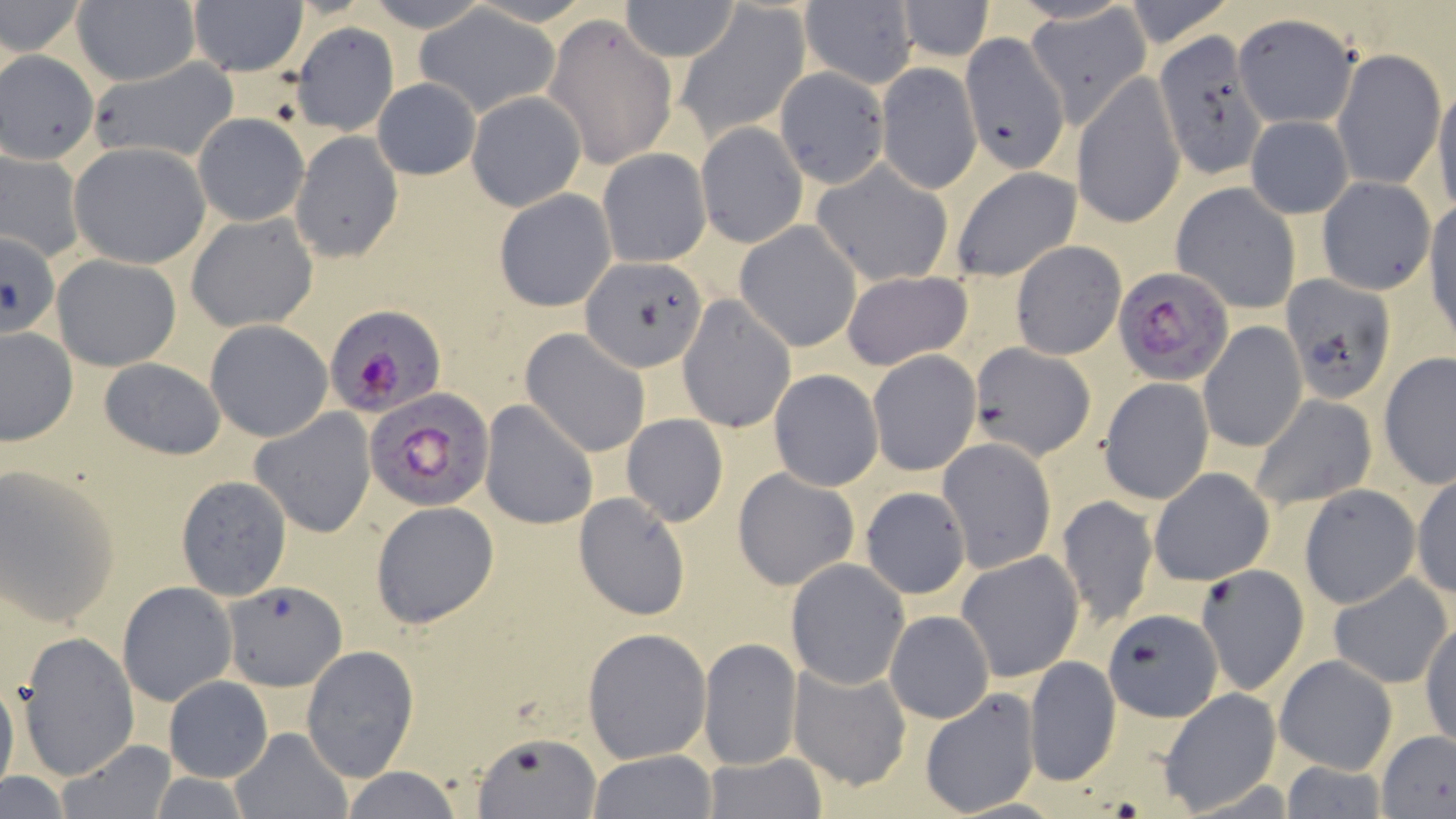
Summary:
  - Coordinate format: approximate bounding boxes as (x1, y1, x2, y2) in pixels
  - Uninfected red blood cell locations: (70, 0, 199, 86), (188, 0, 308, 77), (358, 0, 499, 32), (1120, 0, 1235, 49), (0, 1, 87, 59), (617, 1, 743, 61), (897, 1, 994, 61), (799, 2, 916, 87), (676, 4, 809, 139), (1023, 5, 1153, 127), (416, 8, 559, 118), (1232, 13, 1359, 130), (542, 14, 677, 169), (294, 21, 402, 138), (1150, 35, 1265, 180), (934, 39, 1074, 212), (1332, 48, 1444, 191), (86, 60, 240, 164), (876, 62, 982, 194), (774, 66, 894, 190), (1074, 73, 1185, 229), (371, 77, 481, 179), (1433, 79, 1456, 217), (467, 90, 585, 210), (192, 112, 307, 226), (1244, 114, 1353, 218), (696, 122, 808, 247), (290, 130, 403, 262), (69, 142, 210, 269), (0, 146, 84, 264), (597, 148, 711, 268), (811, 162, 954, 286), (948, 164, 1083, 282), (1317, 177, 1436, 294), (1172, 182, 1302, 315), (494, 188, 615, 312), (1425, 199, 1456, 343), (186, 212, 319, 333), (735, 221, 862, 352), (1, 231, 60, 339), (1011, 240, 1125, 358), (51, 254, 182, 370), (581, 257, 706, 372), (841, 269, 972, 370), (1281, 275, 1396, 404), (677, 294, 797, 433), (206, 319, 333, 441), (1199, 322, 1306, 453), (1, 327, 76, 446), (520, 330, 651, 458), (968, 342, 1094, 461), (867, 349, 981, 476), (1378, 353, 1456, 486), (98, 358, 226, 459), (768, 369, 883, 491), (1100, 377, 1215, 503), (1248, 393, 1377, 511), (480, 399, 599, 529), (250, 408, 378, 538), (621, 414, 728, 526), (938, 438, 1056, 574), (0, 465, 120, 629), (732, 466, 861, 591), (1148, 467, 1274, 586), (1410, 472, 1455, 598), (175, 476, 292, 600), (1299, 484, 1420, 608), (860, 487, 971, 599), (573, 492, 690, 619), (1057, 493, 1157, 629), (370, 501, 500, 629), (956, 549, 1084, 682), (786, 558, 909, 688), (1197, 564, 1309, 695), (1329, 573, 1451, 688), (118, 582, 236, 707), (223, 584, 350, 693), (1101, 609, 1224, 723), (884, 611, 995, 723), (1420, 620, 1455, 749), (581, 627, 713, 764), (16, 632, 139, 781), (698, 638, 802, 769), (300, 645, 419, 782), (1274, 654, 1397, 774), (1024, 655, 1120, 787), (787, 659, 911, 791), (0, 675, 19, 798), (163, 676, 273, 783), (918, 688, 1040, 815), (1159, 688, 1281, 813), (226, 727, 352, 818), (1376, 729, 1456, 819), (472, 730, 602, 819), (56, 739, 179, 818), (586, 750, 719, 818), (700, 753, 828, 819), (1276, 760, 1394, 816), (341, 766, 464, 819), (0, 773, 71, 817)
  - Plasmodium falciparum-infected red blood cell locations: (1113, 266, 1235, 386), (325, 306, 445, 417), (364, 389, 495, 512)
  - Slide-level diagnosis: Plasmodium falciparum
  - Stain: May-Grünwald-Giemsa
  - Magnification: 1000x
  - Preparation: thin blood film
  - Image size: 1456×819 pixels
  - Modality: light microscopy
  - Field of view: single